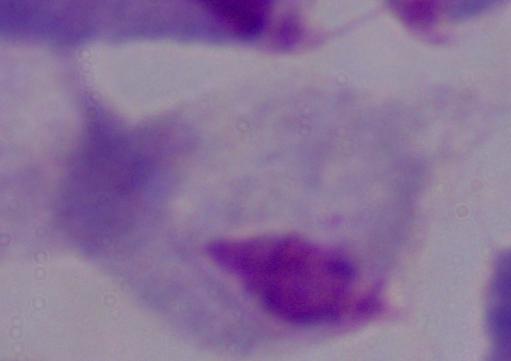
Summary:
  - Modality: photomicrograph
  - Magnification: 1000x
  - Identification: trichomonad